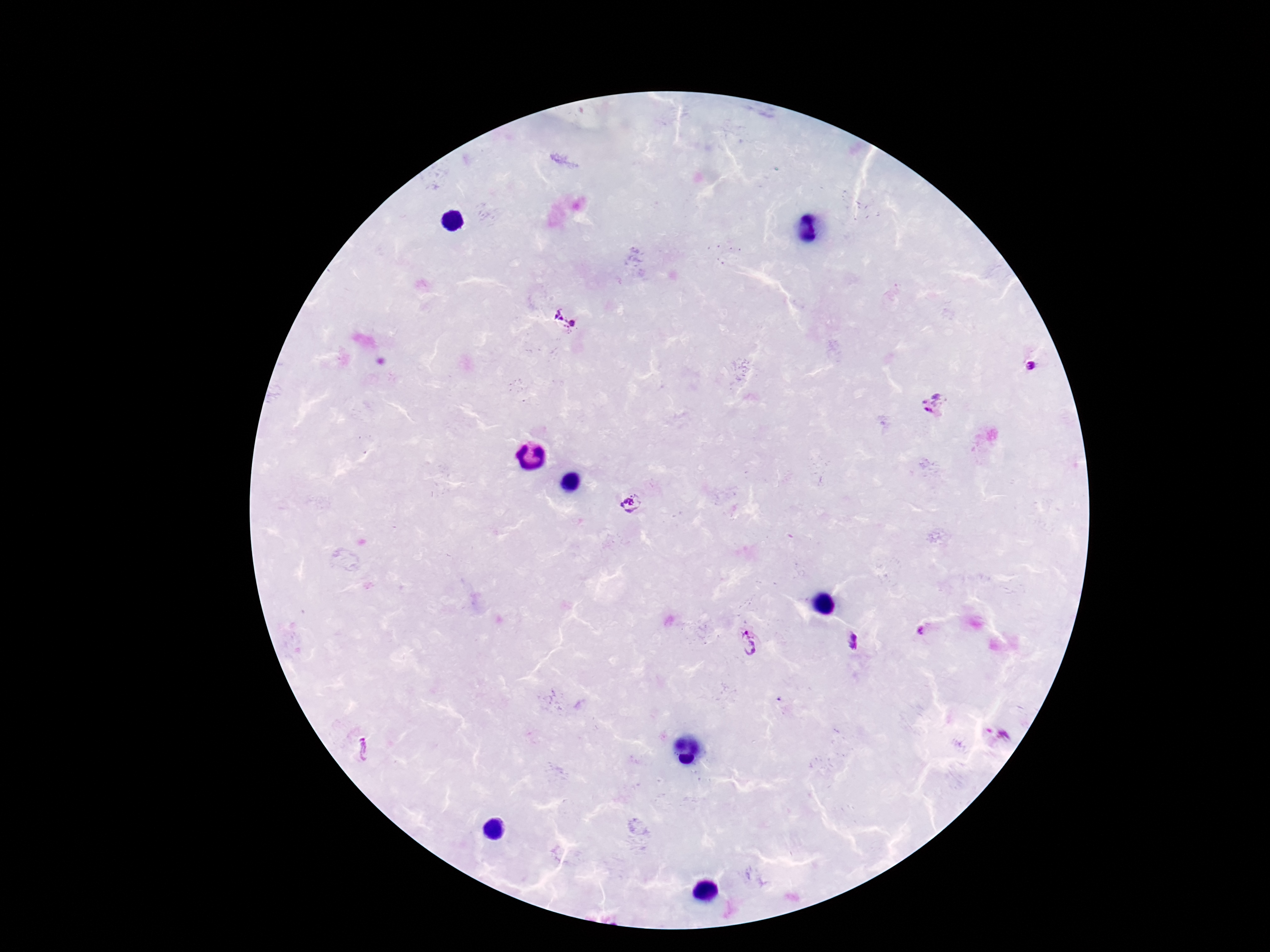
Plasmodium parasite locations = approximate object centers, in pixels from the top-left corner: (x=557, y=315), (x=573, y=322), (x=1033, y=370), (x=932, y=406), (x=632, y=502), (x=919, y=631), (x=856, y=641), (x=748, y=644), (x=363, y=750)
stain = Giemsa
image size = 1270×952 pixels
preparation = thick peripheral-blood smear
capture = smartphone camera through the microscope eyepiece
magnification = 100x
field of view = single
patient malaria status = positive